Locate every leukocyte (white blood cell).
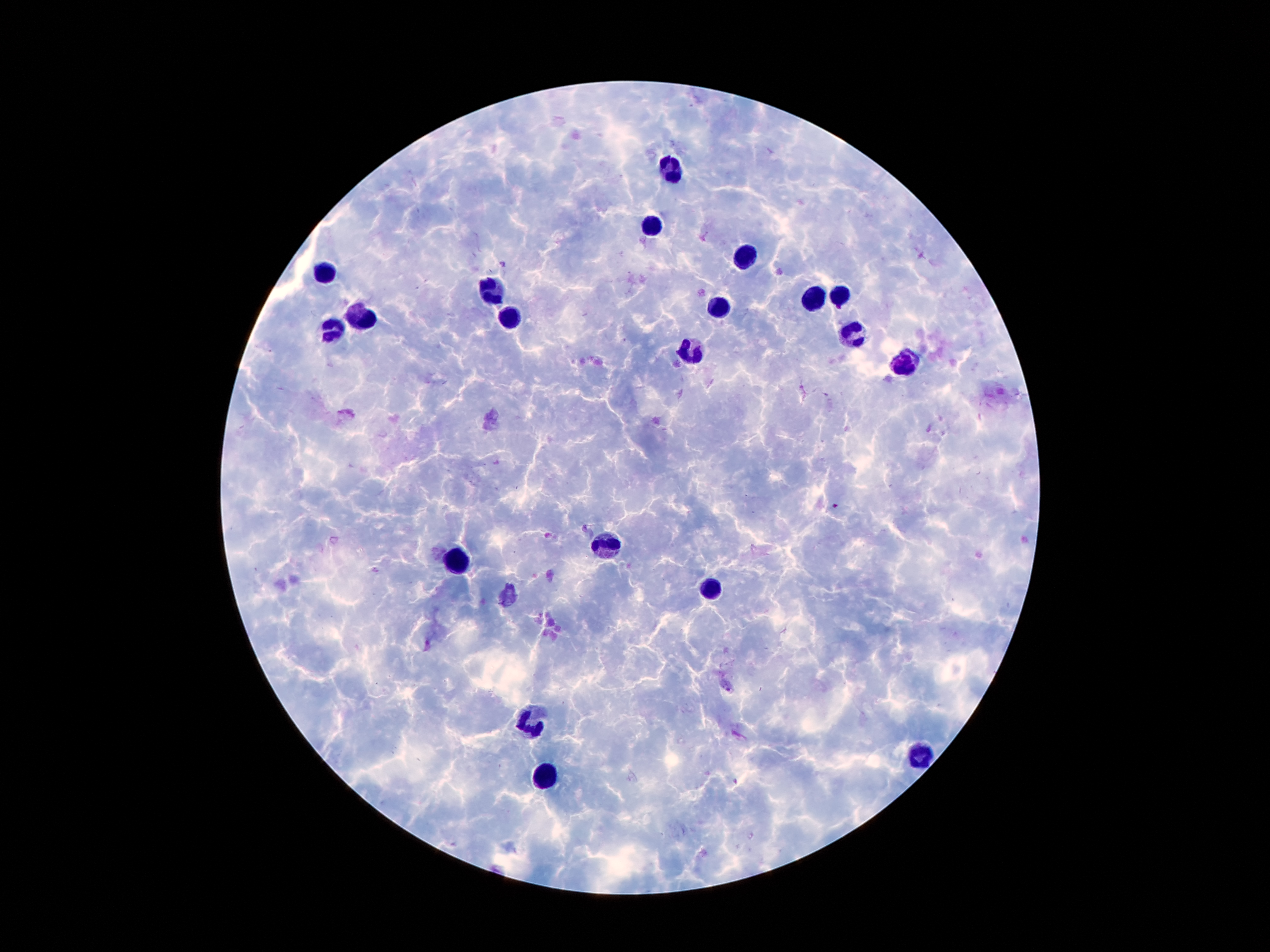
Approximate centers as {x, y} in pixels.
Leukocytes: {671, 171}, {652, 226}, {742, 258}, {326, 270}, {493, 290}, {840, 296}, {814, 301}, {722, 302}, {371, 318}, {514, 319}, {334, 327}, {850, 333}, {693, 356}, {905, 363}, {609, 547}, {458, 562}, {711, 589}, {534, 719}, {922, 754}, {549, 775}.

Summary:
  - Plasmodium parasite locations: {835, 506}
  - Capture: smartphone camera through the microscope eyepiece
  - Field of view: one from this slide
  - Stain: Giemsa
  - Image size: 1270×952 pixels
  - Patient malaria status: positive for Plasmodium falciparum
  - Magnification: 100x
  - Preparation: thick blood film